Report the malaria status of this cell.
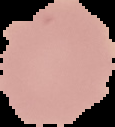
It is uninfected.

Summary:
  - Image type: segmented cell region on a black background
  - Image size: 115×127 pixels
  - Preparation: thin blood smear